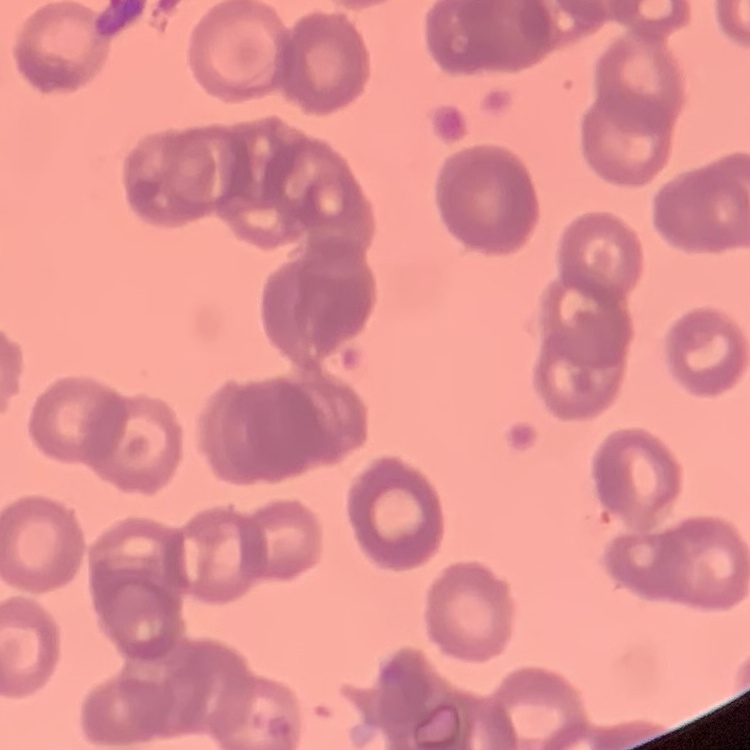
Summary:
  - Red blood cell morphology: rouleaux formation
  - Stain: Field's or Giemsa
  - Preparation: thin blood smear
  - Image type: square crop of a larger photomicrograph